Classify this cell by malaria status.
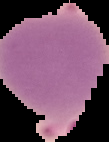
Parasitized.

preparation = thin blood film
image size = 109×142 pixels
image type = segmented cell region with the area outside set to black